Assess this cell for malaria.
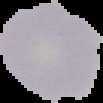

Uninfected.

Summary:
  - Image type: cell region segmented out of the field of view; surrounding area masked to black
  - Preparation: thin blood film
  - Image size: 103×103 pixels